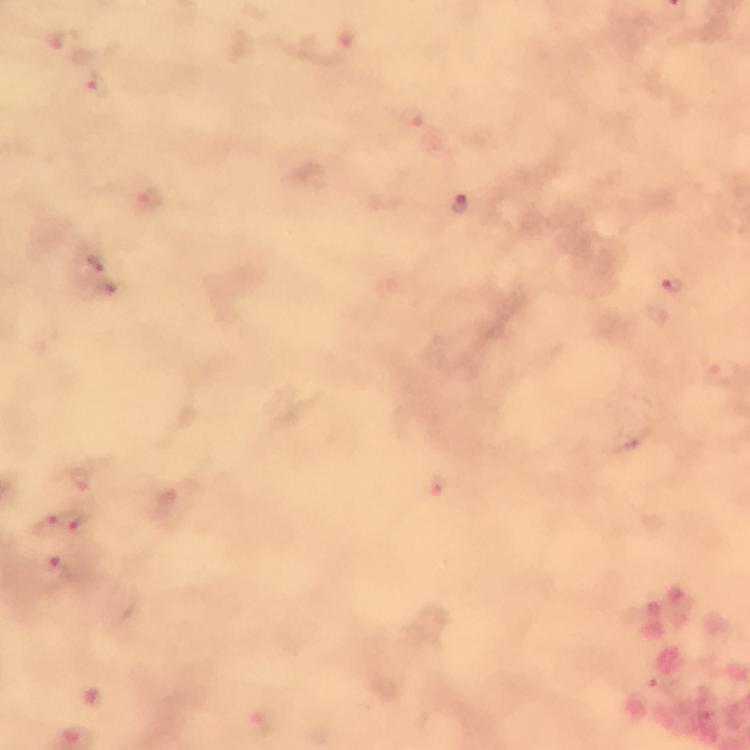

{
  "stain": "Giemsa",
  "context": "from a malaria diagnostic workup",
  "capture": "smartphone photograph through a microscope",
  "magnification": "100x",
  "preparation": "thick smear",
  "plasmodium_parasite_locations": "approximate centers as (x, y) in pixels: (59, 37), (99, 87), (412, 117), (147, 199), (460, 203), (94, 260), (673, 284), (78, 478), (441, 486), (76, 523), (44, 525), (53, 571)",
  "image_size": "750×750 pixels",
  "immersion_oil": "applied",
  "cropped_from": "a single field of view"
}